Locate every leukocyte (white blood cell).
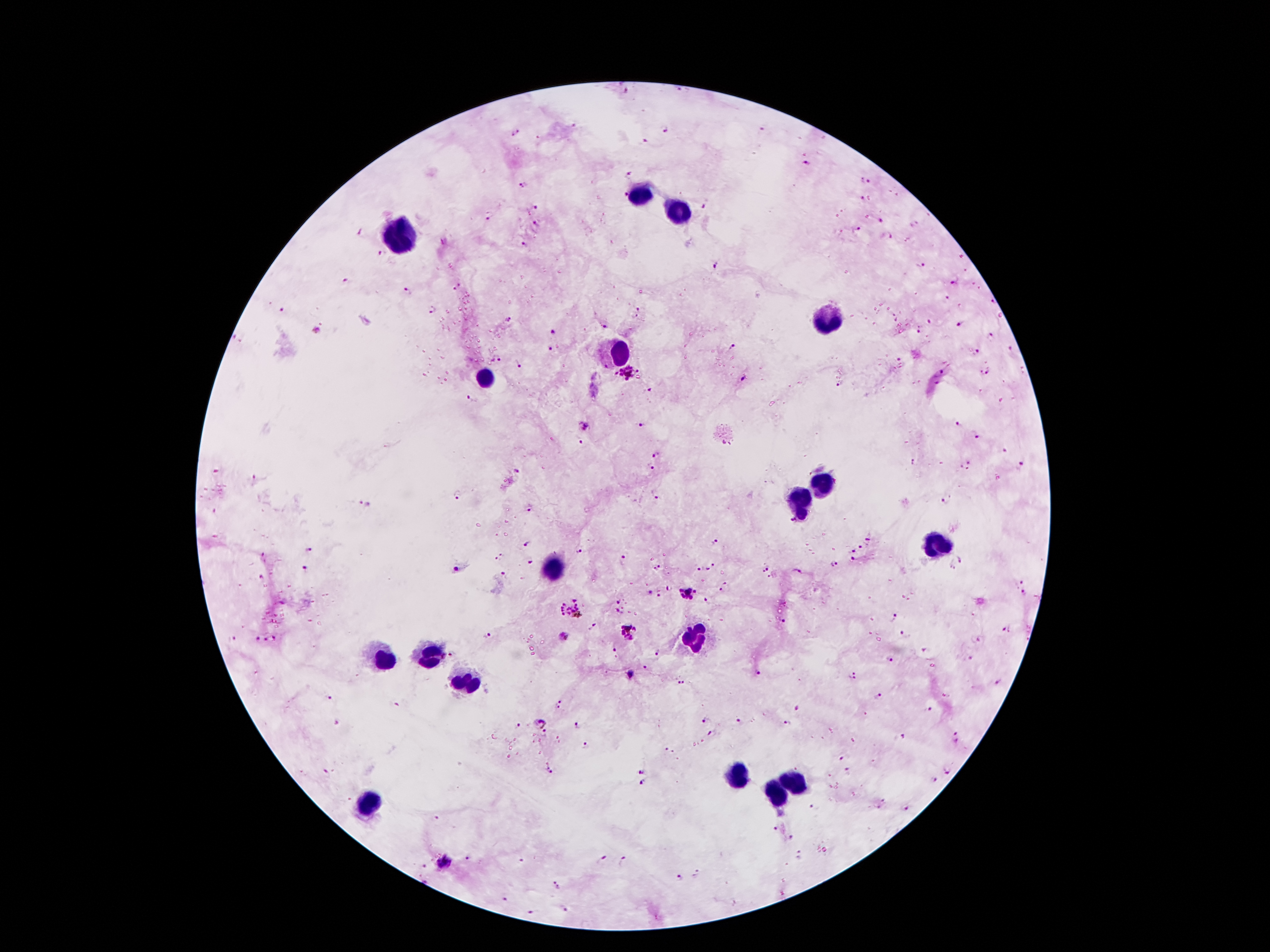

Approximate centers as [x, y] in pixels.
Leukocytes: [639, 193], [681, 212], [400, 237], [828, 319], [620, 349], [483, 378], [823, 483], [799, 501], [933, 546], [555, 570], [694, 638], [431, 657], [387, 660], [463, 680], [735, 777], [793, 784], [775, 792], [371, 800].

Summary:
  - Plasmodium parasite locations: [625, 91], [575, 126], [761, 129], [663, 131], [516, 134], [646, 141], [808, 165], [628, 173], [864, 180], [523, 187], [622, 195], [896, 196], [862, 199], [536, 208], [704, 209], [489, 219], [880, 222], [537, 224], [856, 229], [362, 232], [889, 237], [524, 246], [378, 253], [963, 256], [920, 265], [716, 267], [965, 271], [346, 280], [953, 282], [973, 284], [458, 286], [980, 289], [408, 291], [947, 298], [992, 302], [959, 305], [283, 310], [431, 310], [640, 311], [999, 316], [893, 318], [509, 321], [929, 321], [960, 324], [605, 327], [918, 329], [552, 332], [991, 337], [734, 347], [550, 349], [1011, 350], [974, 354], [496, 360], [901, 362], [520, 366], [985, 371], [940, 373], [628, 377], [742, 378], [840, 383], [647, 390], [470, 398], [586, 424], [641, 425], [957, 426], [974, 437], [581, 441], [1004, 452], [657, 455], [914, 463], [1023, 464], [965, 465], [652, 467], [518, 472], [255, 478], [458, 494], [657, 497], [944, 501], [362, 502], [531, 508], [792, 521], [868, 540], [716, 541], [526, 545], [861, 546], [853, 548], [308, 550], [577, 551], [263, 555], [503, 555], [621, 556], [854, 558], [962, 559], [498, 560], [531, 562], [834, 564], [952, 566], [712, 567], [457, 568], [765, 568], [304, 569], [658, 569], [698, 569], [797, 570], [503, 575], [261, 578], [1023, 581], [726, 587], [669, 588], [648, 592], [689, 593], [1023, 593], [658, 595], [619, 600], [708, 601], [573, 610], [618, 611], [895, 617], [783, 622], [594, 626], [1004, 629], [628, 631], [904, 634], [565, 636], [235, 638], [257, 638], [276, 639], [486, 639], [979, 640], [265, 641], [615, 646], [925, 649], [658, 651], [450, 653], [969, 658], [890, 660], [646, 668], [758, 672], [631, 673], [853, 675], [683, 682], [999, 682], [878, 695], [328, 699], [394, 704], [559, 705], [929, 708], [798, 709], [706, 719], [738, 720], [335, 722], [788, 722], [539, 723], [519, 725], [575, 726], [545, 734], [712, 735], [903, 736], [957, 736], [587, 747], [669, 752], [840, 758], [551, 770], [643, 770], [847, 771], [947, 771], [326, 772], [933, 778], [643, 783], [883, 800], [814, 807], [878, 807], [908, 809], [438, 816], [776, 828], [791, 837], [800, 854], [468, 858], [602, 858], [623, 859], [521, 860], [445, 863], [423, 866], [697, 873], [678, 877], [557, 886], [508, 897], [563, 907], [531, 911]
  - Field of view: one from this slide
  - Preparation: thick blood film
  - Patient malaria status: positive for Plasmodium falciparum
  - Capture: smartphone through the microscope eyepiece
  - Magnification: 100x
  - Stain: Giemsa
  - Image size: 1270×952 pixels